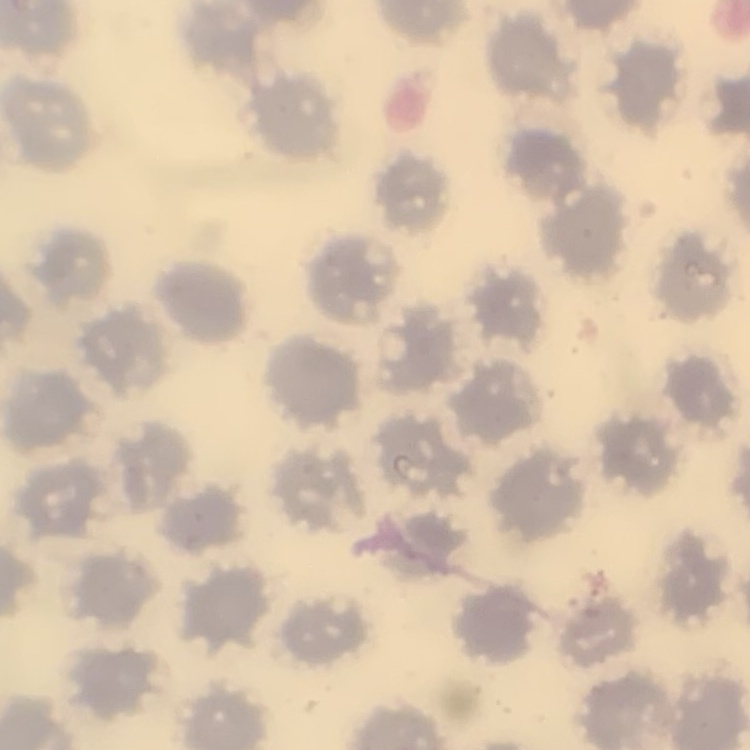
{
  "erythrocyte_morphology": "no rouleaux formation",
  "image_type": "one tile cut from a larger photomicrograph",
  "stain": "Field's or Giemsa",
  "preparation": "thin blood film"
}